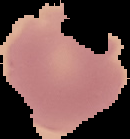

From a thin blood film. Image is 130×139 pixels. Result: no malaria parasites seen. Cell region segmented out of the field of view; the surrounding area is masked to black.